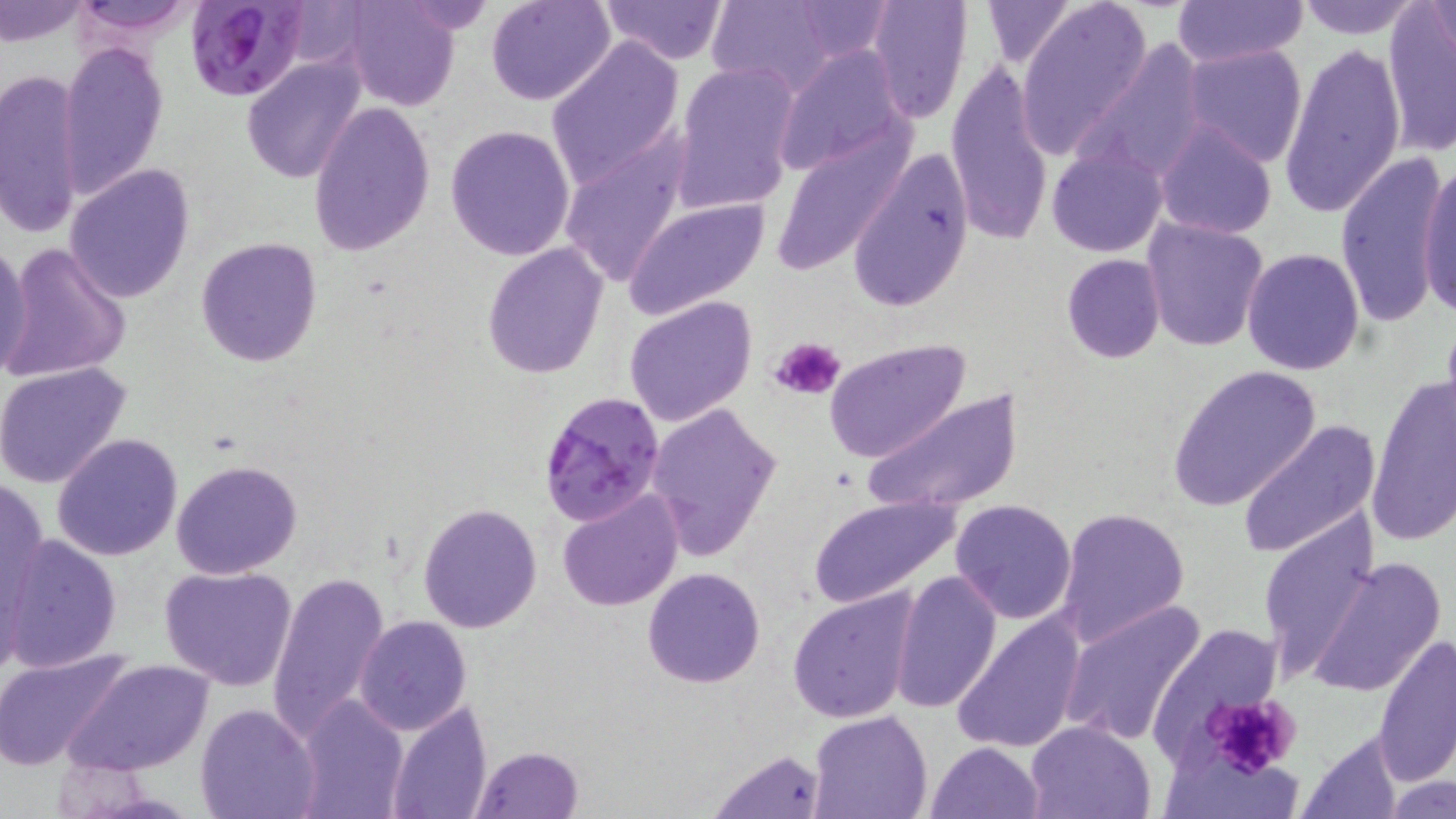

slide-level diagnosis = Plasmodium falciparum
magnification = 1000x
stain = May-Grünwald-Giemsa
modality = light microscopy
uninfected red blood cell locations = approximate bounding boxes as [x1, y1, x2, y2] in pixels: [0, 0, 90, 49], [67, 0, 205, 38], [487, 0, 618, 106], [599, 0, 729, 66], [706, 0, 841, 94], [788, 0, 899, 60], [866, 0, 974, 124], [978, 0, 1078, 68], [1171, 0, 1308, 69], [1294, 0, 1425, 38], [337, 1, 462, 111], [1017, 1, 1153, 150], [1426, 2, 1456, 61], [1379, 7, 1456, 155], [1277, 37, 1405, 222], [545, 38, 683, 185], [1077, 38, 1210, 183], [59, 39, 168, 198], [773, 43, 912, 177], [1179, 43, 1308, 168], [240, 56, 367, 185], [945, 57, 1054, 245], [673, 60, 800, 212], [0, 65, 86, 241], [306, 100, 436, 257], [1155, 119, 1276, 240], [444, 125, 576, 260], [772, 130, 912, 277], [558, 134, 693, 287], [1046, 145, 1167, 257], [847, 146, 975, 314], [1334, 151, 1451, 326], [1417, 157, 1456, 318], [65, 164, 195, 304], [623, 197, 773, 322], [1141, 217, 1270, 354], [193, 235, 323, 369], [0, 239, 34, 380], [482, 241, 607, 379], [1, 242, 132, 383], [1242, 247, 1366, 376], [1060, 253, 1167, 364], [624, 295, 757, 429], [824, 338, 971, 463], [0, 360, 132, 489], [1168, 364, 1323, 513], [1367, 375, 1455, 542], [861, 389, 1026, 516], [645, 400, 783, 562], [1235, 419, 1381, 560], [50, 433, 183, 560], [171, 458, 301, 578], [1, 473, 49, 646], [556, 489, 683, 611], [806, 495, 960, 608], [948, 498, 1077, 622], [418, 502, 543, 632], [1055, 507, 1190, 646], [1254, 514, 1375, 677], [2, 538, 122, 671], [1306, 555, 1448, 699], [159, 564, 299, 689], [642, 567, 766, 688], [890, 567, 1000, 712], [268, 571, 389, 741], [787, 586, 919, 725], [1059, 597, 1208, 747], [950, 609, 1088, 755], [354, 615, 472, 734], [1145, 623, 1288, 765], [1372, 632, 1455, 786], [0, 649, 132, 770], [62, 658, 214, 778], [294, 695, 410, 817], [383, 699, 493, 818], [196, 702, 322, 819], [807, 711, 931, 819], [1024, 719, 1158, 819], [1296, 729, 1407, 818], [924, 740, 1047, 819], [470, 746, 584, 819], [708, 746, 831, 819], [1385, 775, 1453, 819]
Plasmodium falciparum-infected red blood cell locations = approximate bounding boxes as [x1, y1, x2, y2] in pixels: [185, 1, 311, 104], [538, 391, 668, 525]
preparation = thin blood film
field of view = single
platelet locations = approximate bounding boxes as [x1, y1, x2, y2] in pixels: [770, 336, 848, 401], [1203, 690, 1302, 778]
image size = 1456×819 pixels